Locate every Plasmodium falciparum-infected red blood cell.
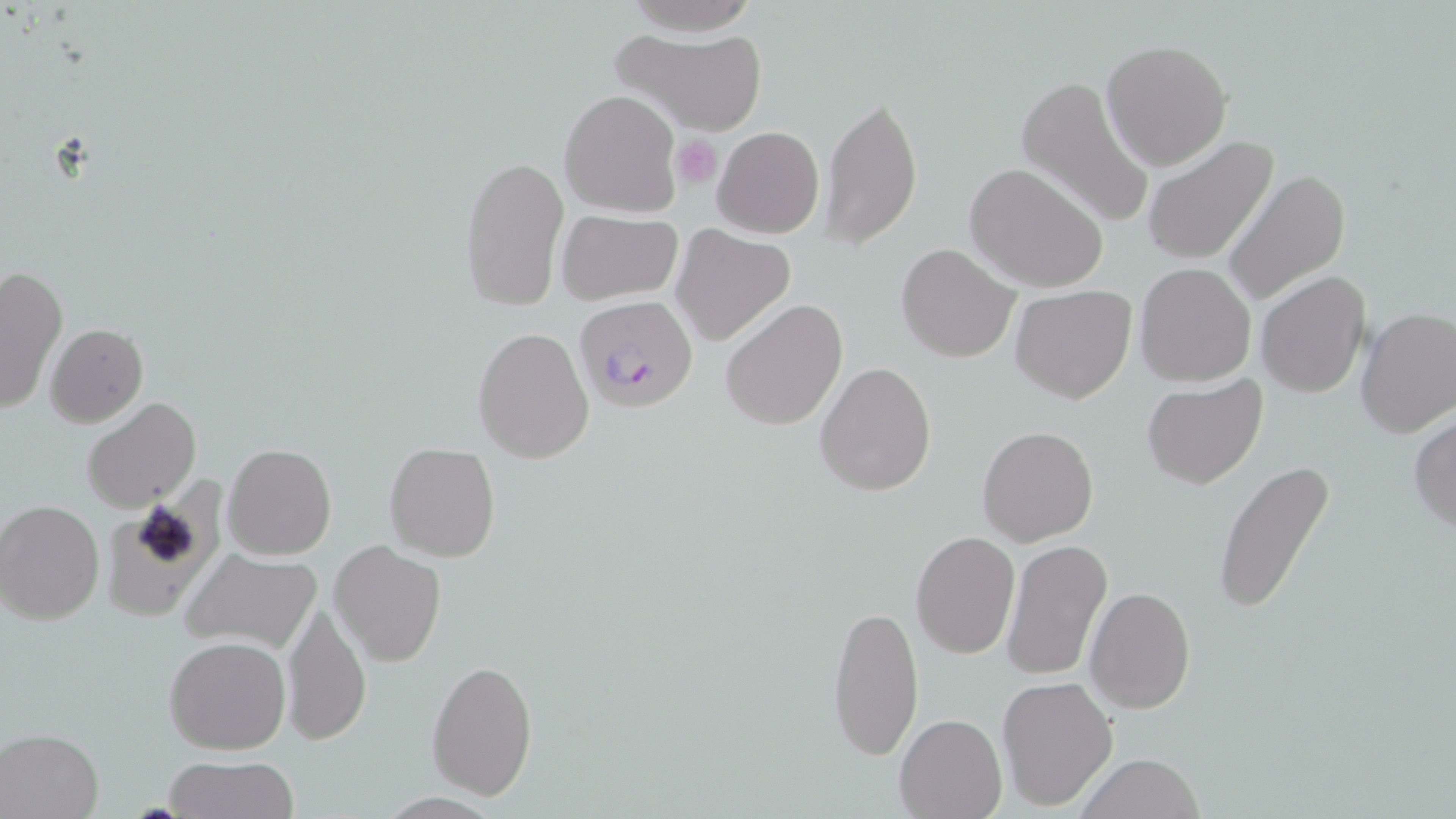
Approximate bounding boxes as [x1, y1, x2, y2] in pixels.
Plasmodium falciparum-infected red blood cells: [574, 296, 698, 413].

slide-level diagnosis = Plasmodium falciparum
preparation = thin blood film
stain = May-Grünwald-Giemsa
uninfected red blood cell locations = approximate bounding boxes as [x1, y1, x2, y2] in pixels: [616, 30, 768, 134], [1102, 40, 1233, 173], [1015, 74, 1153, 230], [560, 90, 680, 216], [821, 92, 923, 249], [699, 121, 815, 340], [712, 126, 825, 239], [1143, 134, 1278, 266], [460, 153, 568, 313], [964, 162, 1107, 292], [1222, 170, 1351, 304], [555, 208, 682, 306], [672, 226, 797, 347], [896, 242, 1020, 362], [1135, 263, 1255, 386], [0, 265, 66, 414], [1255, 271, 1371, 398], [1012, 284, 1135, 402], [721, 298, 847, 430], [1355, 308, 1456, 437], [45, 324, 148, 427], [474, 326, 594, 462], [814, 361, 937, 497], [1143, 375, 1269, 490], [81, 396, 200, 512], [1409, 413, 1456, 534], [978, 426, 1098, 545], [224, 442, 337, 560], [385, 443, 499, 562], [1213, 459, 1337, 612], [106, 477, 229, 627], [0, 499, 104, 624], [911, 531, 1020, 658], [1001, 538, 1113, 682], [330, 541, 446, 667], [179, 548, 323, 655], [1084, 587, 1194, 712], [829, 600, 924, 764], [283, 602, 369, 746], [164, 635, 289, 754], [427, 657, 538, 800], [997, 675, 1118, 811], [896, 714, 1006, 819], [1, 727, 104, 819], [1074, 753, 1208, 819], [165, 755, 296, 819]
image size = 1456×819 pixels
modality = light microscopy
magnification = 1000x
field of view = single
platelet locations = approximate bounding boxes as [x1, y1, x2, y2] in pixels: [671, 134, 722, 188]